Assess the morphology of the erythrocytes.
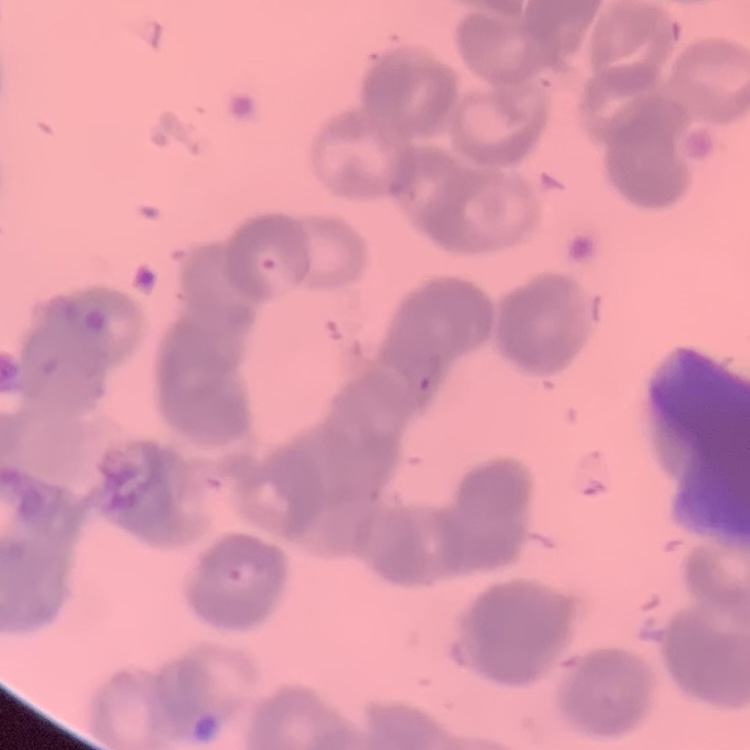
Rouleaux formation.

preparation = thin peripheral smear
image type = square crop of a larger photomicrograph
stain = Field's or Giemsa